State which parasite is depicted.
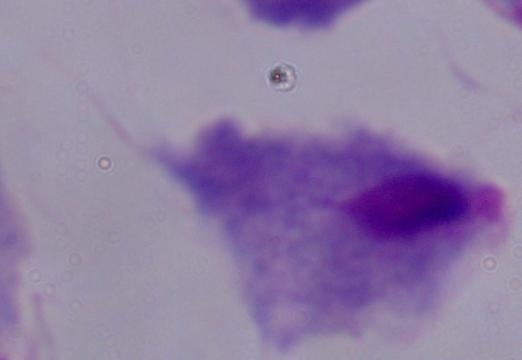

A trichomonad.

{
  "magnification": "1000x",
  "modality": "photomicrograph"
}